Classify this cell by malaria status.
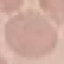

It is uninfected.

Giemsa-stained preparation. Photographed with a smartphone camera at the microscope eyepiece. Automatically extracted cell patch, resized to 64 × 64 pixels. Thin blood film.